Assess this cell for malaria.
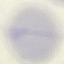
It is uninfected.

stain: Giemsa
capture: smartphone camera at the microscope eyepiece
image_type: cell patch, automatically extracted from a larger field of view and resized to 64 × 64 pixels
preparation: thin blood film